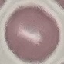
result = no malaria parasites detected
preparation = thin blood smear
capture = smartphone camera at the microscope eyepiece
image type = automatically extracted cell patch, resized to 64 × 64 pixels
stain = Giemsa